Classify this cell by malaria status.
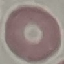
It is uninfected.

preparation = thin blood smear
image type = automatically extracted cell patch, resized to 64 × 64 pixels
stain = Giemsa
capture = smartphone camera at the microscope eyepiece